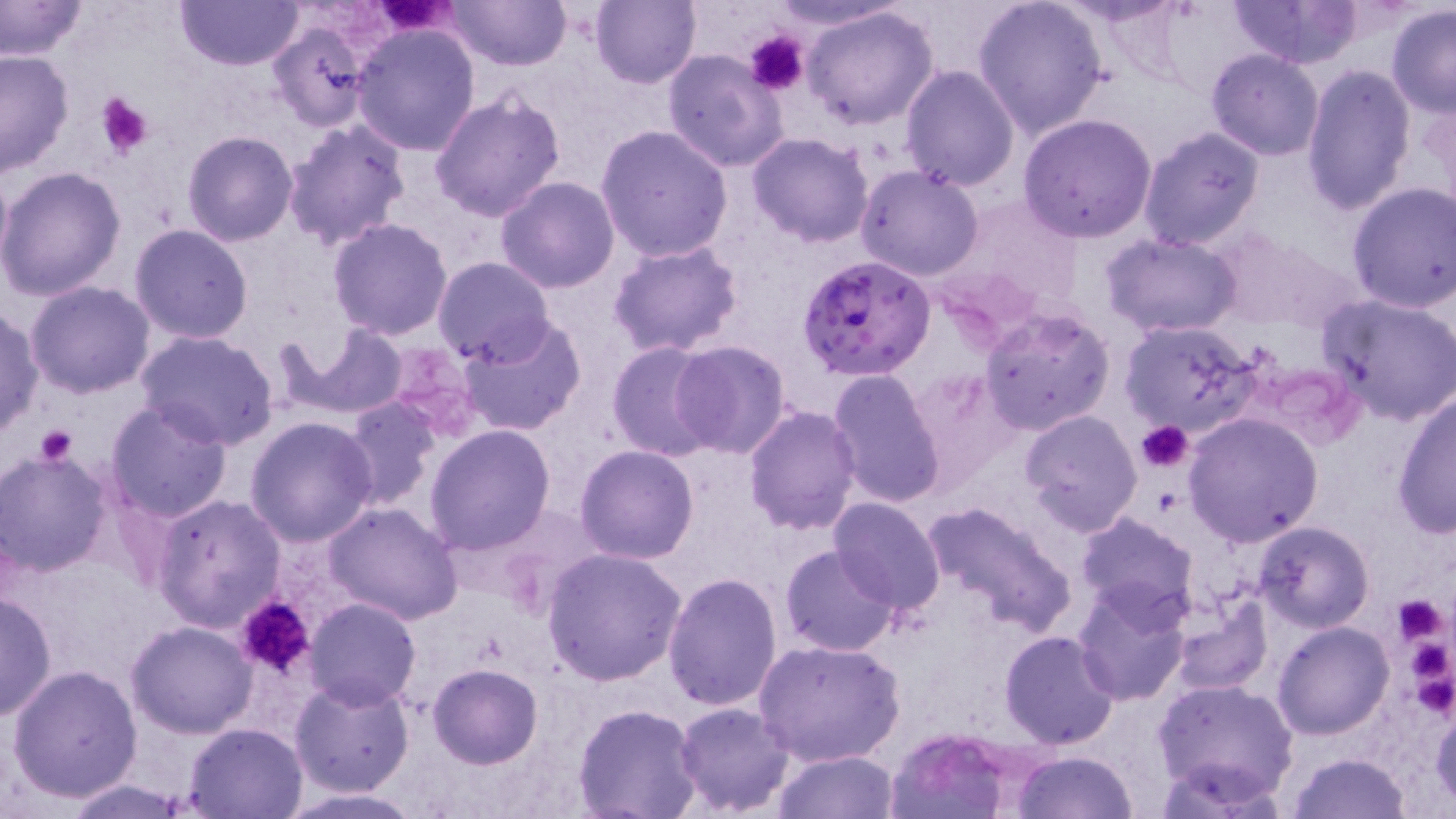 Approximate bounding boxes as (x1, y1, x2, y2) in pixels. Plasmodium falciparum-infected red blood cell locations: (796, 253, 935, 383). Platelet locations: (375, 0, 456, 36), (744, 31, 809, 95), (95, 92, 153, 160), (1136, 420, 1192, 472), (37, 424, 77, 465), (1393, 596, 1450, 646), (234, 597, 318, 680). Uninfected red blood cell locations: (0, 0, 89, 63), (175, 0, 306, 71), (447, 0, 569, 70), (591, 0, 702, 89), (764, 0, 909, 32), (971, 0, 1110, 139), (1227, 0, 1363, 68), (1386, 3, 1456, 118), (802, 5, 940, 131), (266, 21, 370, 132), (350, 22, 481, 155), (0, 48, 75, 177), (662, 49, 788, 172), (1207, 49, 1327, 161), (1300, 63, 1417, 215), (899, 64, 1020, 191), (429, 87, 565, 222), (1019, 113, 1158, 244), (282, 117, 411, 248), (594, 125, 735, 263), (1137, 126, 1265, 252), (182, 130, 300, 246), (747, 132, 873, 244), (855, 163, 984, 280), (0, 166, 127, 300), (495, 177, 620, 293), (1345, 181, 1456, 313), (951, 197, 1081, 310), (328, 216, 454, 339), (129, 225, 254, 344), (1212, 232, 1362, 336), (1102, 234, 1247, 339), (608, 242, 744, 357), (432, 257, 557, 366), (25, 281, 155, 399), (1319, 293, 1456, 424), (980, 305, 1115, 434), (0, 308, 43, 439), (459, 316, 588, 437), (1118, 319, 1259, 435), (287, 325, 409, 417), (136, 329, 279, 450), (669, 340, 792, 460), (606, 341, 724, 461), (381, 342, 485, 441), (826, 368, 946, 509), (903, 371, 1022, 496), (1391, 391, 1455, 537), (340, 397, 440, 508), (104, 399, 234, 522), (744, 404, 862, 535), (1020, 410, 1141, 535), (1181, 412, 1324, 546), (245, 416, 379, 546), (425, 424, 556, 554), (574, 445, 700, 564), (0, 450, 115, 578), (152, 493, 285, 634), (827, 497, 947, 617), (920, 498, 1078, 640), (322, 501, 463, 625), (1075, 512, 1200, 625), (1253, 521, 1375, 633), (780, 544, 900, 657), (543, 548, 685, 687), (662, 571, 783, 709), (1072, 584, 1193, 706), (1172, 589, 1271, 695), (0, 591, 56, 723), (304, 598, 420, 711), (126, 620, 257, 737), (1273, 621, 1393, 739), (999, 630, 1120, 749), (752, 637, 905, 769), (427, 662, 543, 768), (6, 664, 142, 802), (289, 676, 415, 797), (1153, 678, 1299, 804), (1430, 697, 1455, 809), (673, 702, 796, 817), (574, 704, 704, 819), (182, 721, 308, 817), (886, 729, 1024, 819), (1009, 749, 1139, 819), (772, 750, 899, 819), (1288, 753, 1412, 819), (58, 778, 197, 817), (274, 787, 430, 818). Slide-level diagnosis: Plasmodium falciparum. Optical microscopy. One field of a larger specimen. Image is 1456×819 pixels. May-Grünwald-Giemsa-stained preparation. Thin blood film. Captured at 1000x magnification.